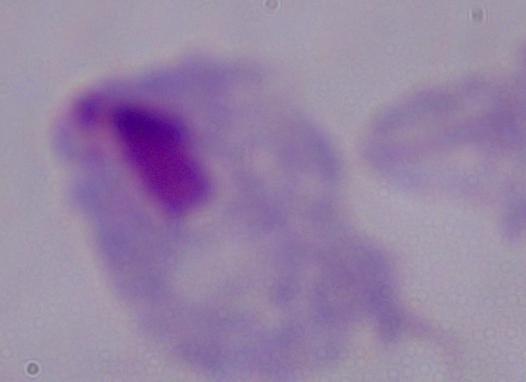

Photomicrograph. A trichomonad is seen. 1000x magnification.